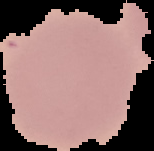
Cell region segmented out of the field of view; the surrounding area is masked to black. Result: no malaria parasites detected. Image is 154×151 pixels. From a thin blood film.